Identify the parasite.
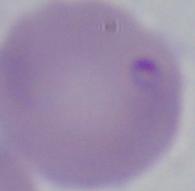

Babesia.

{
  "modality": "photomicrograph",
  "magnification": "1000x"
}